Outline each blood parasite and name the species.
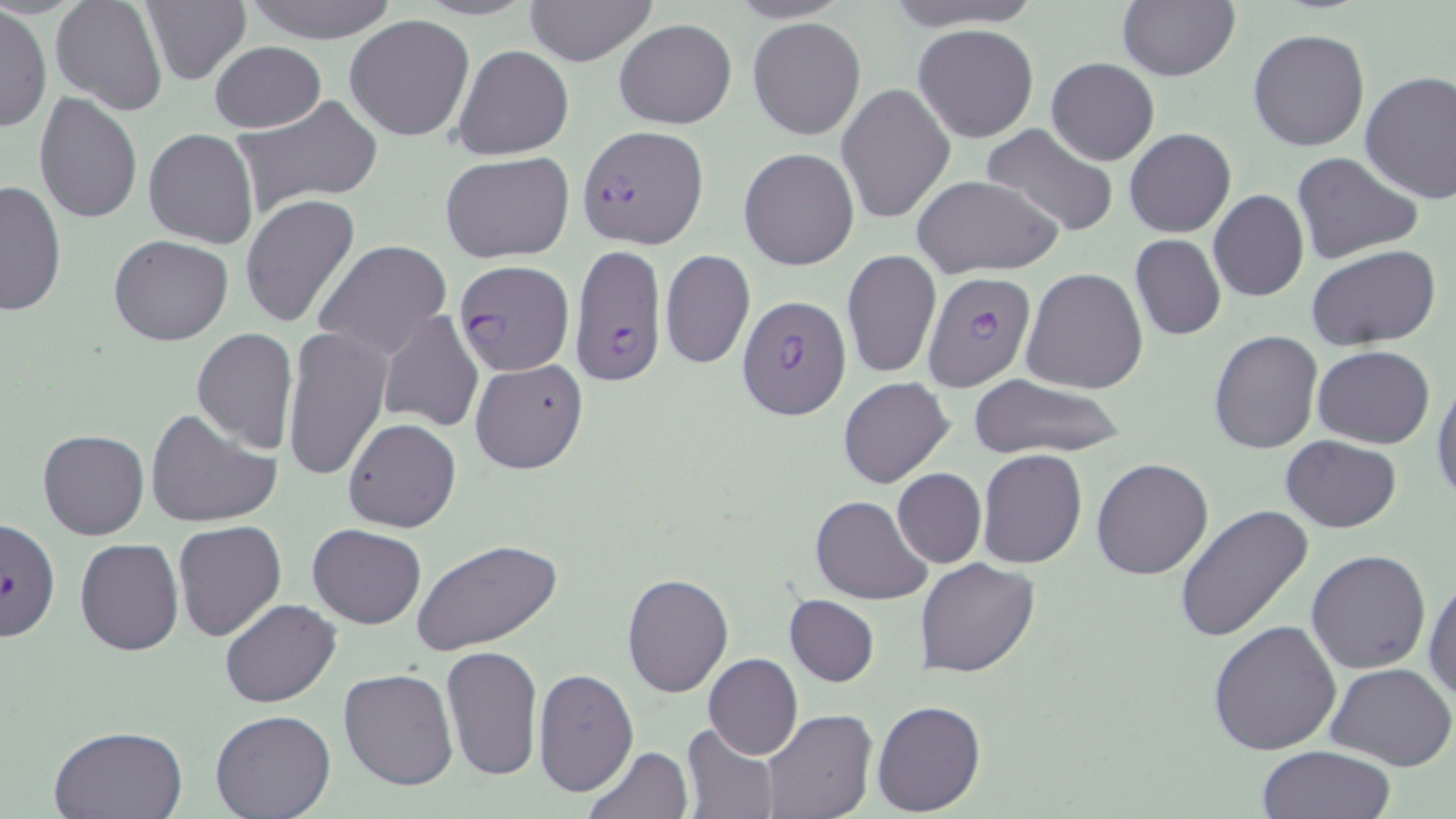
Approximate bounding boxes as (x1, y1, x2, y2) in pixels.
Plasmodium falciparum-infected red blood cells: (577, 124, 707, 249), (570, 246, 667, 385), (456, 259, 575, 376), (921, 270, 1037, 392), (735, 295, 853, 421), (1, 518, 62, 641).
No Plasmodium ovale, Plasmodium malariae, Plasmodium vivax, Babesia divergens, or Trypanosoma brucei observed.

Uninfected red blood cell locations: (50, 0, 167, 116), (238, 0, 400, 44), (522, 0, 658, 67), (880, 0, 1044, 30), (139, 2, 251, 85), (1116, 2, 1240, 82), (1, 8, 50, 134), (343, 14, 476, 141), (748, 17, 867, 141), (614, 19, 736, 129), (912, 24, 1039, 142), (1247, 28, 1370, 151), (209, 41, 325, 133), (452, 45, 574, 161), (1048, 57, 1159, 165), (1359, 71, 1456, 204), (838, 82, 955, 225), (35, 92, 143, 223), (229, 97, 382, 218), (978, 124, 1121, 238), (1125, 128, 1235, 237), (142, 129, 259, 249), (739, 148, 859, 270), (439, 150, 574, 264), (1293, 152, 1422, 263), (911, 175, 1062, 277), (0, 179, 67, 317), (1208, 190, 1308, 303), (241, 194, 361, 329), (1130, 234, 1225, 341), (107, 235, 234, 347), (314, 241, 453, 359), (1307, 246, 1440, 347), (659, 249, 755, 370), (842, 250, 940, 379), (1022, 267, 1149, 395), (376, 309, 485, 432), (281, 325, 392, 482), (190, 327, 299, 453), (1209, 329, 1324, 455), (1314, 346, 1435, 449), (469, 359, 589, 475), (1432, 375, 1456, 507), (966, 376, 1128, 458), (838, 377, 954, 489), (146, 408, 281, 529), (343, 419, 461, 533), (38, 430, 149, 539), (1280, 436, 1402, 532), (977, 449, 1087, 569), (1091, 458, 1214, 580), (892, 468, 986, 568), (810, 496, 931, 605), (1174, 505, 1313, 643), (173, 519, 288, 641), (307, 524, 426, 629), (411, 537, 562, 654), (75, 538, 183, 656), (1306, 549, 1431, 675), (917, 558, 1038, 678), (621, 572, 734, 698), (1424, 573, 1456, 704), (784, 595, 879, 686), (220, 598, 341, 708), (1208, 619, 1343, 757), (440, 644, 545, 782), (704, 654, 802, 759), (1327, 662, 1456, 769), (534, 666, 639, 798), (338, 668, 458, 792), (871, 700, 986, 817), (760, 709, 875, 819), (211, 711, 336, 819), (682, 723, 781, 818), (49, 724, 189, 817), (581, 746, 691, 819), (1258, 746, 1395, 819). Slide-level diagnosis: Plasmodium falciparum. Captured at 1000x magnification. Image is 1456×819 pixels. Thin blood film. Optical microscopy. Single field of view. May-Grünwald-Giemsa-stained preparation.